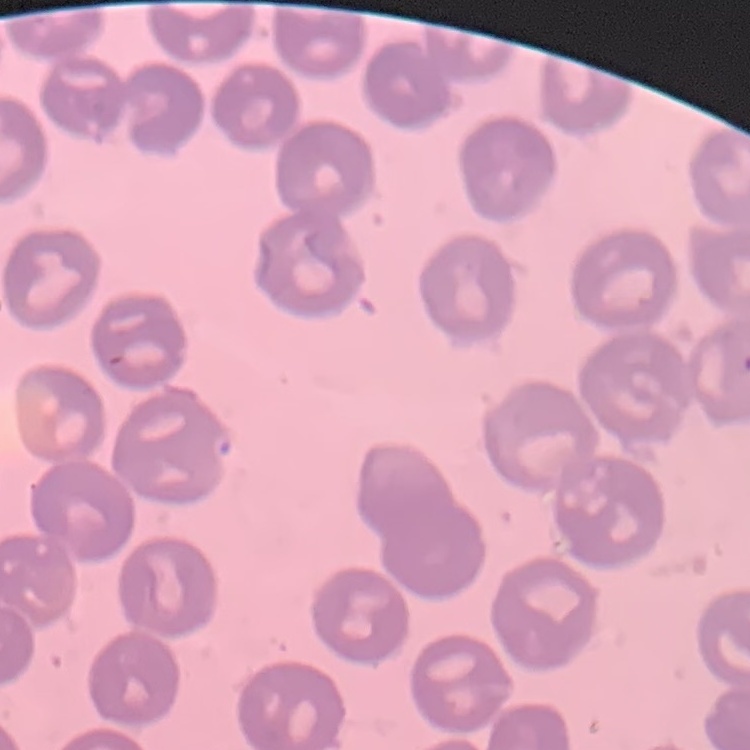

The erythrocytes exhibit no rouleaux formation. Square crop of a larger photomicrograph. Thin blood smear. Stained with either Field's or Giemsa.